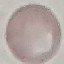

Summary:
  - Malaria status: uninfected
  - Capture: smartphone camera at the microscope eyepiece
  - Preparation: thin blood smear
  - Image type: cell patch, automatically extracted from a larger field of view and resized to 64 × 64 pixels
  - Stain: Giemsa